Assess the morphology of the erythrocytes.
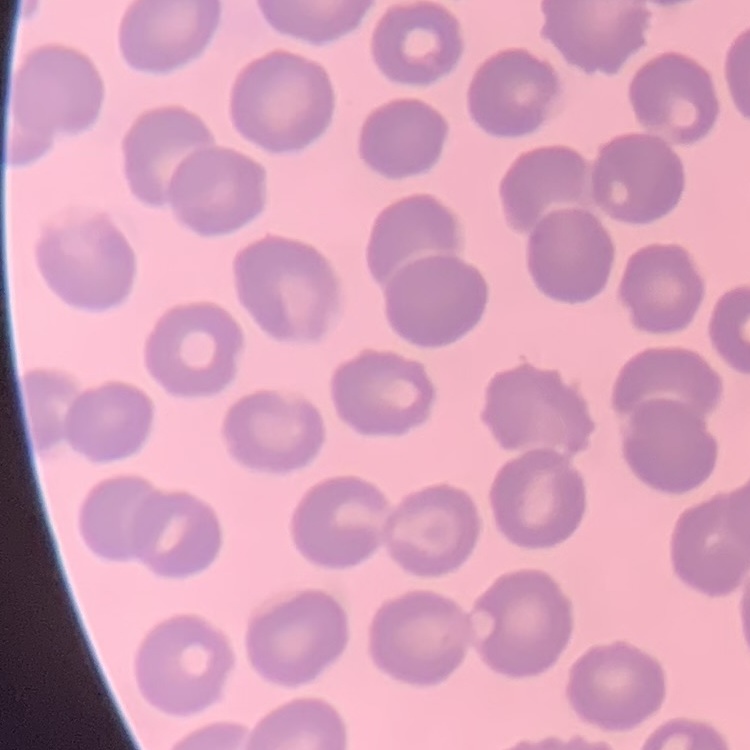
They show no rouleaux formation.

Stained with either Field's or Giemsa. Thin peripheral smear. Square crop of a larger photomicrograph.